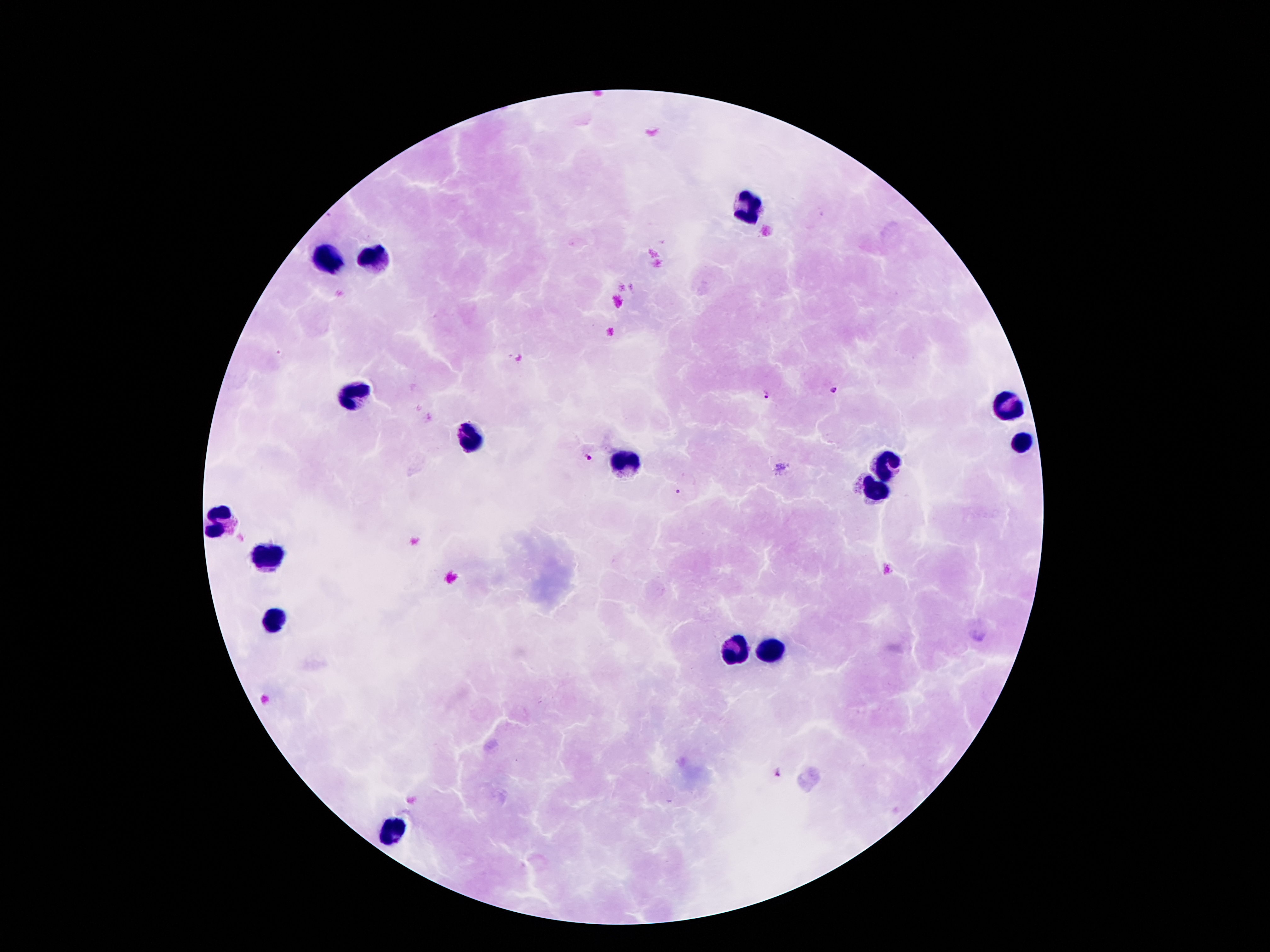
field_of_view: single
capture: smartphone through the microscope eyepiece
leukocyte_locations: 'approximate centers as [x, y] in pixels: [743, 207], [325, 256], [372, 259], [355, 397], [1008, 409], [469, 434], [1022, 444], [622, 464], [882, 469], [877, 491], [219, 515], [271, 555], [276, 622], [768, 651], [736, 654], [394, 829]'
plasmodium_parasite_locations: 'approximate centers as [x, y] in pixels: [832, 389], [766, 393], [588, 455], [678, 491], [780, 774]'
preparation: thick blood smear
stain: Giemsa
image_size: 1270×952 pixels
magnification: 100x
patient_malaria_status: infected with Plasmodium falciparum